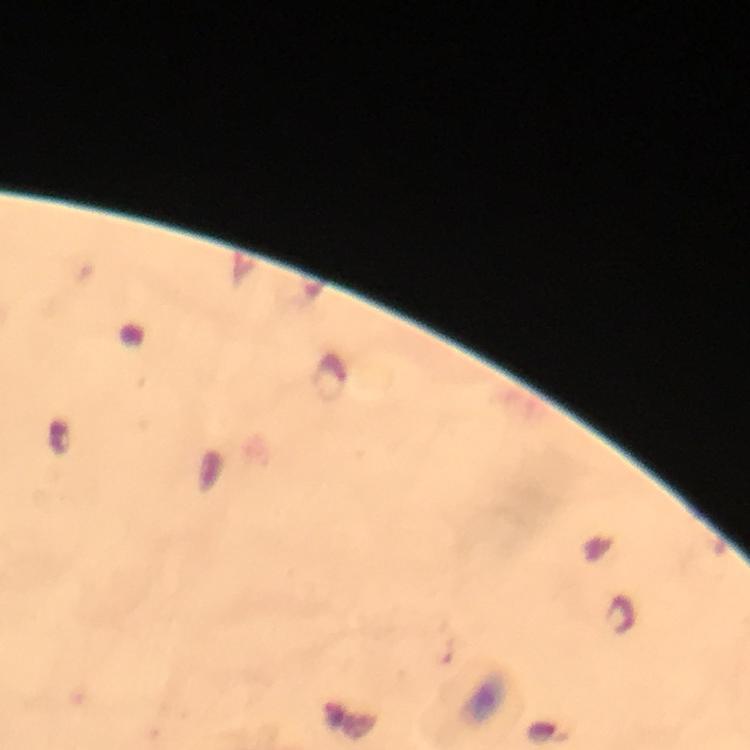

cropped_from: a single field of view
capture: smartphone mounted on the microscope
context: from a malaria diagnostic workup
stain: Giemsa
magnification: 100x
image_size: 750×750 pixels
preparation: thick blood film
malaria_parasite_locations: 'approximate centers as [x, y] in pixels: [331, 374]'
immersion_oil: used